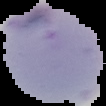
Summary:
  - Malaria status: parasitized
  - Image size: 106×106 pixels
  - Image type: cell region segmented out of the field of view; surrounding area masked to black
  - Preparation: thin blood film